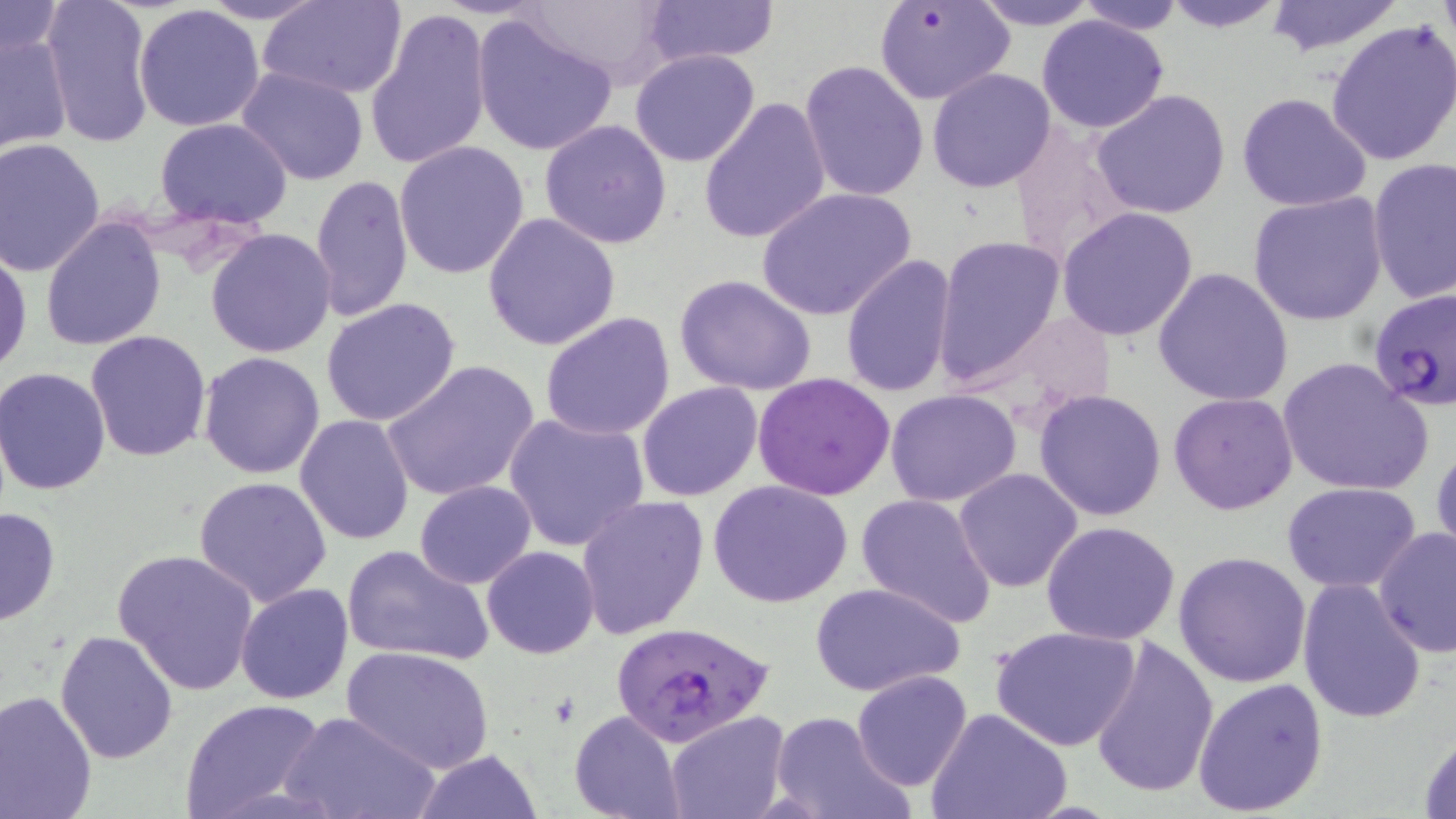
Summary:
  - Coordinate format: approximate bounding boxes as (x1, y1, x2, y2) in pixels
  - Uninfected red blood cell locations: (42, 0, 155, 148), (194, 0, 333, 25), (261, 0, 408, 99), (642, 0, 780, 67), (874, 0, 1015, 106), (964, 0, 1105, 30), (1154, 0, 1292, 32), (1260, 0, 1406, 57), (1073, 1, 1188, 35), (1, 2, 68, 66), (516, 3, 675, 89), (134, 4, 267, 132), (365, 8, 492, 172), (471, 14, 618, 158), (1037, 14, 1169, 134), (1326, 20, 1456, 166), (0, 27, 73, 155), (630, 49, 762, 167), (799, 60, 928, 201), (236, 67, 369, 186), (926, 68, 1057, 193), (1090, 89, 1232, 220), (1236, 92, 1373, 211), (697, 95, 832, 246), (154, 118, 294, 227), (539, 119, 673, 249), (1006, 121, 1139, 271), (0, 139, 105, 276), (394, 141, 530, 280), (1366, 158, 1456, 304), (311, 174, 414, 323), (756, 188, 919, 324), (1247, 193, 1389, 325), (1057, 207, 1200, 341), (481, 213, 622, 351), (40, 217, 166, 353), (206, 228, 337, 358), (933, 234, 1066, 388), (0, 245, 31, 376), (841, 254, 958, 398), (1153, 266, 1295, 407), (673, 273, 817, 395), (1369, 288, 1456, 416), (320, 298, 462, 428), (968, 310, 1118, 417), (538, 312, 677, 441), (85, 331, 213, 463), (199, 352, 326, 479), (1277, 357, 1433, 495), (381, 360, 539, 501), (1, 368, 114, 496), (752, 373, 898, 500), (636, 381, 764, 501), (1034, 389, 1168, 521), (884, 390, 1024, 508), (1168, 392, 1299, 515), (502, 411, 649, 553), (295, 413, 416, 544), (1430, 440, 1456, 564), (952, 469, 1084, 592), (192, 477, 334, 607), (414, 481, 537, 589), (710, 481, 853, 609), (1282, 481, 1423, 591), (855, 491, 998, 627), (575, 494, 710, 639), (0, 505, 61, 627), (1041, 520, 1181, 645), (1372, 526, 1455, 657), (342, 544, 495, 667), (482, 546, 598, 658), (112, 548, 260, 695), (1173, 550, 1313, 688), (1296, 578, 1426, 724), (235, 582, 355, 705), (811, 582, 965, 697), (991, 625, 1142, 751), (55, 628, 180, 763), (1088, 636, 1219, 799), (341, 646, 492, 774), (852, 670, 973, 792), (1192, 677, 1328, 816), (0, 689, 100, 818), (180, 698, 328, 818), (927, 709, 1072, 819), (282, 710, 436, 819), (569, 710, 686, 819), (768, 710, 910, 819), (666, 712, 786, 819), (1415, 726, 1456, 819), (410, 748, 545, 819)
  - Plasmodium falciparum-infected red blood cell locations: (610, 620, 774, 746)
  - Slide-level diagnosis: Plasmodium falciparum
  - Stain: May-Grünwald-Giemsa
  - Field of view: single
  - Image size: 1456×819 pixels
  - Preparation: thin blood film
  - Magnification: 1000x
  - Modality: optical microscopy